Identify the blood parasite species.
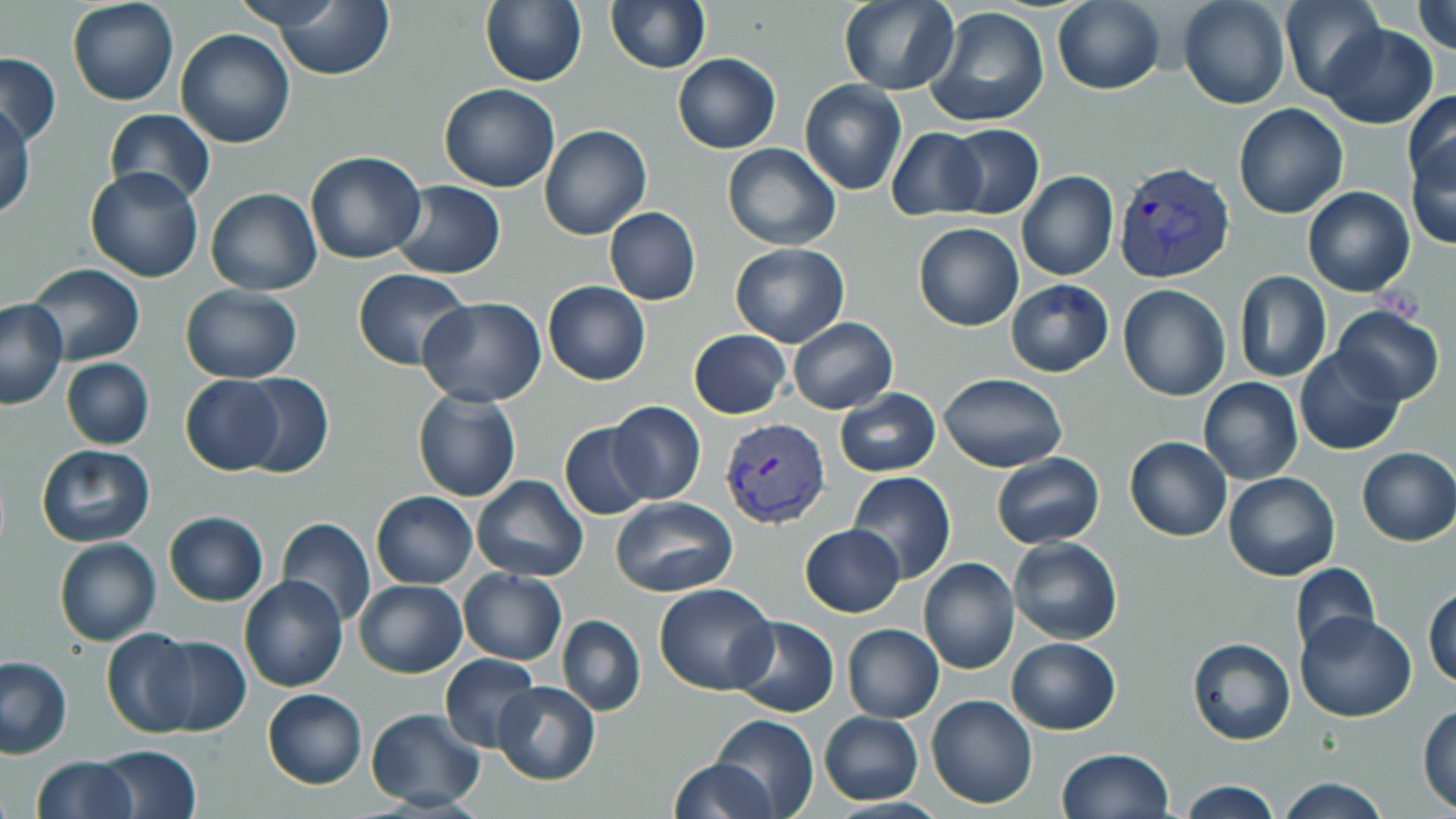
Plasmodium vivax.

Approximate bounding boxes as named x1/y1/x2/y2 corners in pixels. Plasmodium vivax-infected red blood cell locations: (x1=1113, y1=159, x2=1236, y2=285), (x1=719, y1=417, x2=829, y2=528). Uninfected red blood cell locations: (x1=67, y1=0, x2=178, y2=106), (x1=226, y1=0, x2=352, y2=35), (x1=606, y1=0, x2=710, y2=73), (x1=837, y1=0, x2=960, y2=94), (x1=1178, y1=0, x2=1290, y2=109), (x1=1279, y1=0, x2=1386, y2=101), (x1=1411, y1=0, x2=1456, y2=55), (x1=480, y1=2, x2=586, y2=86), (x1=1051, y1=2, x2=1165, y2=93), (x1=274, y1=3, x2=393, y2=81), (x1=925, y1=6, x2=1050, y2=127), (x1=1321, y1=24, x2=1437, y2=127), (x1=175, y1=28, x2=296, y2=147), (x1=1, y1=51, x2=61, y2=147), (x1=673, y1=53, x2=779, y2=153), (x1=799, y1=79, x2=907, y2=195), (x1=440, y1=83, x2=561, y2=192), (x1=1403, y1=89, x2=1456, y2=203), (x1=1233, y1=103, x2=1349, y2=218), (x1=1, y1=105, x2=36, y2=221), (x1=103, y1=108, x2=216, y2=204), (x1=945, y1=124, x2=1044, y2=219), (x1=539, y1=125, x2=650, y2=239), (x1=886, y1=128, x2=986, y2=221), (x1=1405, y1=133, x2=1456, y2=250), (x1=722, y1=143, x2=842, y2=249), (x1=305, y1=149, x2=427, y2=265), (x1=83, y1=167, x2=205, y2=283), (x1=1017, y1=171, x2=1118, y2=281), (x1=392, y1=181, x2=506, y2=278), (x1=1302, y1=186, x2=1415, y2=296), (x1=206, y1=188, x2=322, y2=294), (x1=604, y1=207, x2=701, y2=306), (x1=913, y1=223, x2=1025, y2=331), (x1=729, y1=243, x2=850, y2=347), (x1=23, y1=263, x2=145, y2=365), (x1=353, y1=269, x2=473, y2=369), (x1=1233, y1=270, x2=1331, y2=383), (x1=1006, y1=280, x2=1113, y2=377), (x1=542, y1=282, x2=650, y2=385), (x1=1118, y1=284, x2=1232, y2=401), (x1=180, y1=285, x2=301, y2=381), (x1=418, y1=296, x2=548, y2=405), (x1=0, y1=300, x2=68, y2=410), (x1=1332, y1=304, x2=1444, y2=406), (x1=789, y1=318, x2=896, y2=413), (x1=688, y1=329, x2=791, y2=418), (x1=1295, y1=348, x2=1404, y2=455), (x1=60, y1=358, x2=154, y2=450), (x1=938, y1=373, x2=1066, y2=472), (x1=235, y1=374, x2=333, y2=477), (x1=180, y1=375, x2=284, y2=474), (x1=1199, y1=379, x2=1303, y2=485), (x1=833, y1=388, x2=941, y2=477), (x1=412, y1=391, x2=521, y2=503), (x1=607, y1=401, x2=706, y2=504), (x1=559, y1=422, x2=653, y2=520), (x1=1124, y1=437, x2=1232, y2=542), (x1=36, y1=444, x2=155, y2=547), (x1=1356, y1=447, x2=1455, y2=547), (x1=991, y1=453, x2=1105, y2=548), (x1=847, y1=471, x2=955, y2=583), (x1=1222, y1=471, x2=1340, y2=582), (x1=471, y1=475, x2=589, y2=581), (x1=371, y1=491, x2=477, y2=588), (x1=612, y1=495, x2=738, y2=597), (x1=164, y1=512, x2=268, y2=605), (x1=278, y1=517, x2=376, y2=626), (x1=800, y1=523, x2=905, y2=618), (x1=1007, y1=537, x2=1123, y2=644), (x1=54, y1=538, x2=161, y2=646), (x1=918, y1=557, x2=1020, y2=673), (x1=1290, y1=563, x2=1379, y2=658), (x1=458, y1=569, x2=567, y2=665), (x1=239, y1=574, x2=349, y2=692), (x1=354, y1=579, x2=468, y2=678), (x1=655, y1=584, x2=777, y2=695), (x1=1424, y1=585, x2=1456, y2=691), (x1=1297, y1=612, x2=1417, y2=722), (x1=557, y1=614, x2=645, y2=715), (x1=729, y1=615, x2=839, y2=717), (x1=841, y1=624, x2=945, y2=722), (x1=102, y1=629, x2=197, y2=737), (x1=147, y1=635, x2=250, y2=737), (x1=1187, y1=637, x2=1295, y2=746), (x1=1008, y1=638, x2=1120, y2=734), (x1=439, y1=654, x2=542, y2=751), (x1=0, y1=655, x2=74, y2=759), (x1=493, y1=681, x2=601, y2=785), (x1=262, y1=688, x2=367, y2=788), (x1=926, y1=695, x2=1037, y2=809), (x1=1418, y1=703, x2=1456, y2=813), (x1=366, y1=709, x2=487, y2=811), (x1=820, y1=712, x2=923, y2=805), (x1=711, y1=715, x2=818, y2=819), (x1=90, y1=745, x2=203, y2=818), (x1=1056, y1=749, x2=1174, y2=818), (x1=31, y1=756, x2=137, y2=818), (x1=668, y1=758, x2=776, y2=818), (x1=1275, y1=776, x2=1390, y2=818), (x1=1177, y1=779, x2=1281, y2=819). May-Grünwald-Giemsa stain. Optical microscopy. Thin blood film. Captured at 1000x magnification. Image is 1456×819 pixels. One field of a larger specimen.